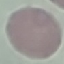
malaria status = uninfected
capture = smartphone through the microscope eyepiece
stain = Giemsa
image type = cell patch, automatically extracted from a larger field of view and resized to 64 × 64 pixels
preparation = thin smear